Outline each uninfected red blood cell.
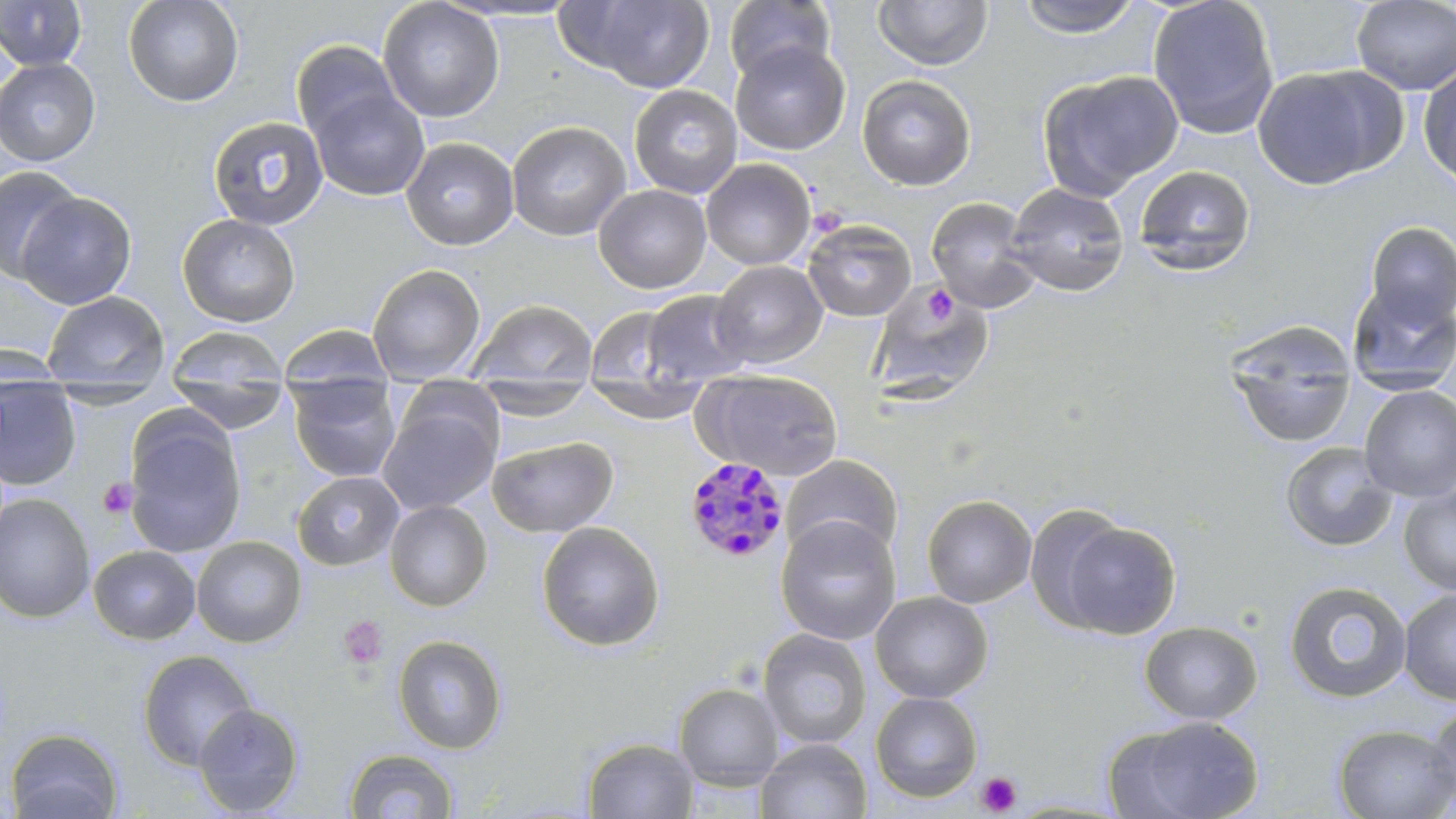
Approximate bounding boxes as (x1,y1)-(x2,y2) corner pairs in pixels.
Uninfected red blood cells: (0,0)-(88,71), (123,0)-(244,107), (377,0)-(504,123), (571,0)-(714,92), (723,0)-(836,85), (1015,0)-(1143,39), (1147,0)-(1281,140), (1351,0)-(1455,95), (873,1)-(993,71), (290,40)-(401,145), (730,41)-(851,156), (0,58)-(101,166), (1418,61)-(1456,191), (1252,65)-(1399,190), (1038,69)-(1184,199), (857,74)-(976,191), (628,84)-(743,198), (308,87)-(430,201), (206,115)-(326,243), (506,120)-(631,241), (401,136)-(520,251), (700,158)-(816,270), (0,164)-(84,281), (1132,165)-(1256,276), (1005,183)-(1131,297), (593,184)-(712,294), (15,190)-(137,310), (925,197)-(1041,313), (176,213)-(301,327), (802,220)-(917,321), (1365,222)-(1456,329), (710,260)-(828,369), (366,263)-(486,385), (867,283)-(995,404), (1347,283)-(1456,393), (41,290)-(170,392), (641,290)-(754,386), (464,298)-(598,389), (584,307)-(685,388), (1225,321)-(1359,449), (277,324)-(395,400), (165,325)-(289,407), (0,343)-(68,386), (693,369)-(845,482), (168,373)-(291,434), (288,376)-(401,483), (583,376)-(710,424), (474,377)-(595,422), (0,380)-(81,491), (1358,386)-(1456,502), (377,400)-(501,516), (124,411)-(246,559), (486,435)-(619,537), (1279,441)-(1399,553), (780,455)-(904,563), (291,471)-(405,571), (1399,483)-(1456,595), (0,493)-(95,623), (921,494)-(1037,608), (384,500)-(492,612), (1025,504)-(1136,633), (775,516)-(902,646), (1056,518)-(1182,640), (536,521)-(665,652), (191,536)-(307,648), (88,545)-(201,645), (1283,580)-(1412,704), (1399,588)-(1456,704), (869,590)-(993,703), (1139,620)-(1262,724), (758,628)-(872,749), (393,635)-(508,755), (138,649)-(259,770), (673,683)-(785,789), (870,692)-(983,802), (192,702)-(304,816), (1424,702)-(1456,809), (1114,715)-(1265,818), (1332,723)-(1456,818), (5,727)-(124,819), (582,737)-(700,819), (755,738)-(871,819), (344,748)-(459,818).

Summary:
  - Plasmodium malariae-infected red blood cell locations: (681,457)-(790,565)
  - Platelet locations: (924,284)-(957,326), (97,478)-(138,519), (339,614)-(388,668), (975,771)-(1022,816)
  - Slide-level diagnosis: Plasmodium malariae
  - Modality: light microscopy
  - Stain: May-Grünwald-Giemsa
  - Preparation: thin blood smear
  - Magnification: 1000x
  - Field of view: one of a larger specimen
  - Image size: 1456×819 pixels